Classify this cell by malaria status.
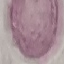

It is uninfected.

Photographed with a smartphone camera at the microscope eyepiece. Thin smear of blood. Automatically extracted cell patch, resized to 64 × 64 pixels. Giemsa stain.